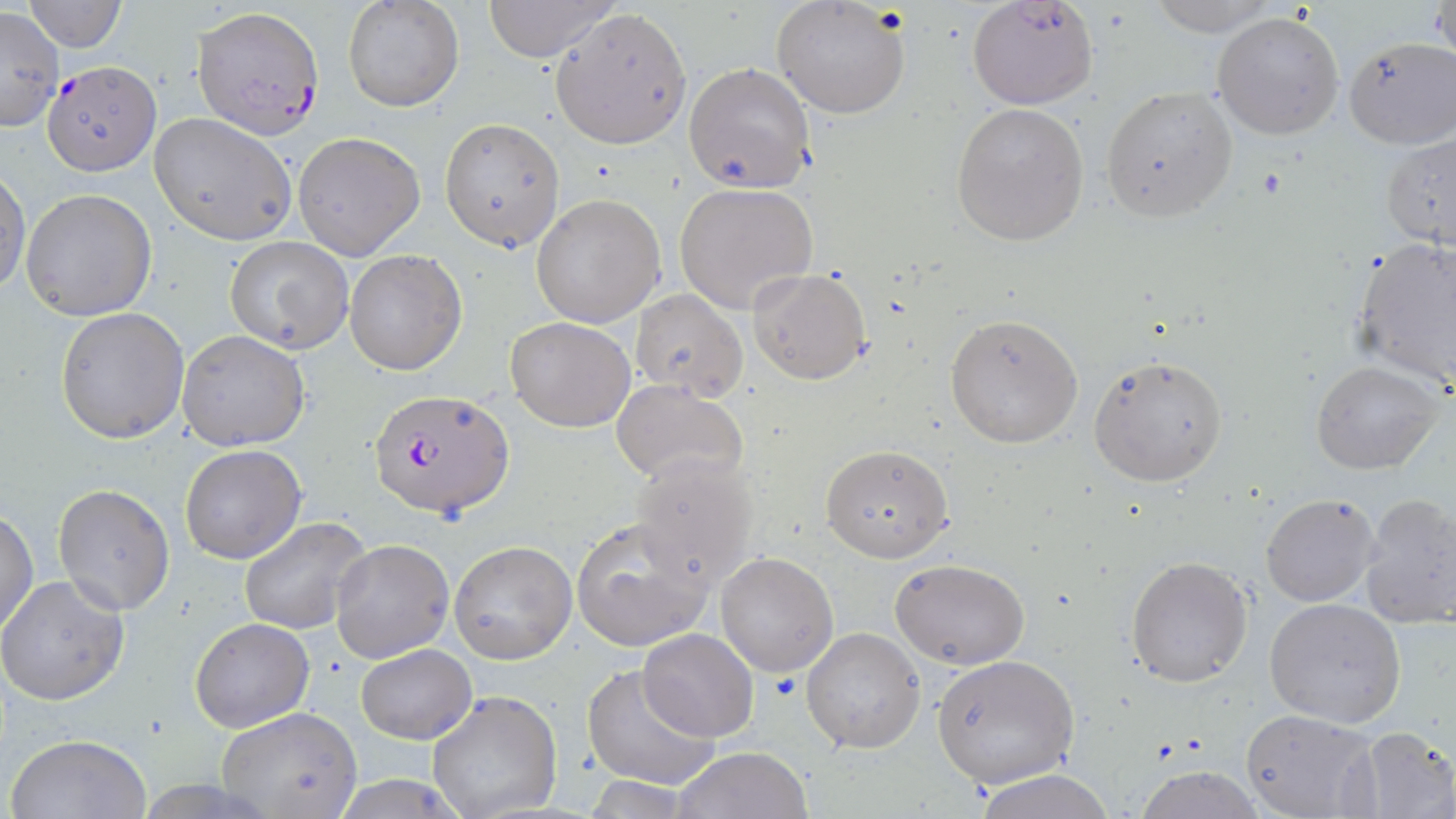
Summary:
  - Coordinate format: approximate bounding boxes as (x1,y1)-(x2,y2) corner pairs in pixels
  - Plasmodium falciparum-infected red blood cell locations: (194,6)-(324,136), (42,60)-(161,174), (368,388)-(514,521)
  - Uninfected red blood cell locations: (25,0)-(126,52), (343,0)-(464,112), (482,0)-(620,63), (771,0)-(911,120), (967,1)-(1098,111), (1140,1)-(1285,36), (1433,1)-(1456,67), (0,7)-(65,130), (551,8)-(692,149), (1211,10)-(1345,140), (1341,35)-(1455,151), (684,61)-(816,193), (1100,87)-(1238,221), (952,103)-(1090,245), (150,111)-(300,246), (440,117)-(566,252), (293,132)-(425,262), (1379,132)-(1455,251), (0,170)-(29,297), (674,183)-(819,313), (20,188)-(157,322), (530,194)-(665,328), (224,235)-(354,353), (1350,237)-(1456,390), (345,249)-(468,375), (748,267)-(870,385), (629,289)-(747,398), (56,308)-(189,444), (945,312)-(1083,449), (505,317)-(636,432), (176,330)-(310,451), (1087,354)-(1228,487), (1311,359)-(1446,475), (611,380)-(747,489), (821,444)-(953,564), (179,445)-(308,565), (630,451)-(761,585), (52,483)-(175,616), (1261,493)-(1380,606), (1358,493)-(1456,629), (1,509)-(38,639), (238,516)-(372,634), (570,518)-(714,652), (330,539)-(455,664), (448,540)-(577,665), (715,552)-(838,676), (1126,555)-(1252,688), (891,559)-(1029,669), (0,577)-(128,706), (1264,597)-(1407,728), (189,619)-(313,734), (802,627)-(925,752), (638,629)-(758,742), (356,643)-(475,745), (931,654)-(1078,788), (581,664)-(720,789), (427,689)-(563,819), (215,706)-(364,817), (1240,708)-(1380,819), (1350,728)-(1456,819), (5,732)-(152,818), (674,747)-(812,819), (1132,766)-(1267,818), (969,768)-(1118,819), (325,776)-(473,817), (581,777)-(701,816)
  - Slide-level diagnosis: Plasmodium falciparum
  - Image size: 1456×819 pixels
  - Preparation: thin blood film
  - Modality: optical microscopy
  - Magnification: 1000x
  - Stain: May-Grünwald-Giemsa
  - Field of view: single